Outline each Plasmodium falciparum-infected red blood cell.
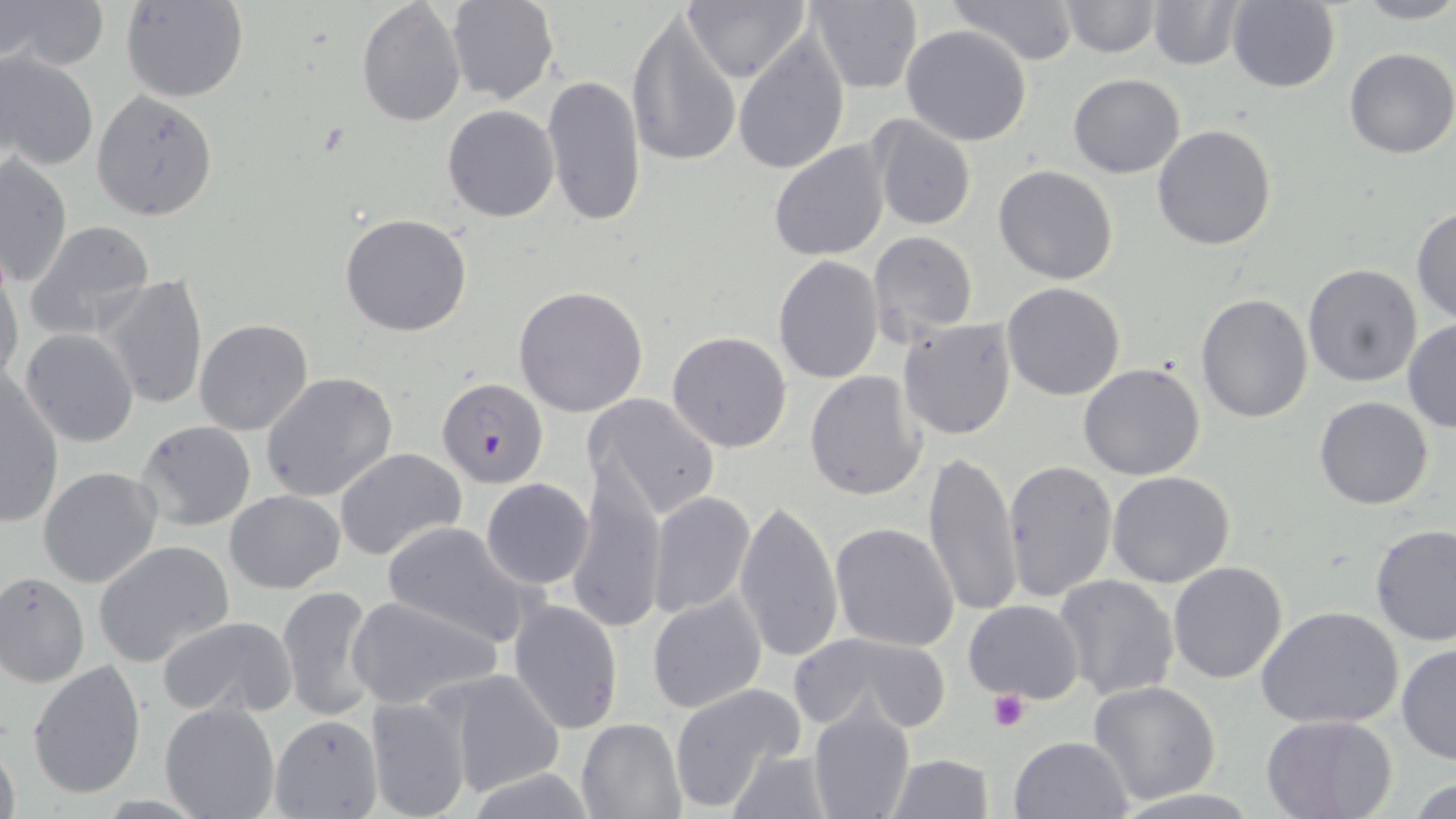
Approximate bounding boxes as named x1/y1/x2/y2 corners in pixels.
Plasmodium falciparum-infected red blood cells (subset): (x1=437, y1=378, x2=549, y2=487).

Uninfected red blood cell locations (subset): (x1=1, y1=0, x2=107, y2=71), (x1=122, y1=0, x2=249, y2=102), (x1=356, y1=0, x2=465, y2=125), (x1=684, y1=0, x2=810, y2=83), (x1=805, y1=0, x2=923, y2=93), (x1=943, y1=0, x2=1080, y2=68), (x1=1058, y1=0, x2=1160, y2=58), (x1=1349, y1=0, x2=1456, y2=25), (x1=447, y1=1, x2=559, y2=104), (x1=1227, y1=1, x2=1342, y2=93), (x1=1149, y1=2, x2=1243, y2=70), (x1=626, y1=10, x2=742, y2=169), (x1=901, y1=23, x2=1032, y2=147), (x1=732, y1=33, x2=850, y2=172), (x1=1344, y1=47, x2=1456, y2=159), (x1=1, y1=50, x2=98, y2=173), (x1=542, y1=72, x2=645, y2=228), (x1=1067, y1=73, x2=1185, y2=178), (x1=90, y1=90, x2=219, y2=221), (x1=442, y1=104, x2=559, y2=222), (x1=867, y1=114, x2=976, y2=230), (x1=1152, y1=124, x2=1277, y2=250), (x1=769, y1=139, x2=891, y2=262), (x1=1, y1=155, x2=72, y2=287), (x1=993, y1=164, x2=1120, y2=285), (x1=1411, y1=207, x2=1456, y2=326), (x1=340, y1=212, x2=473, y2=338), (x1=27, y1=220, x2=155, y2=337), (x1=868, y1=229, x2=978, y2=347), (x1=773, y1=256, x2=884, y2=385), (x1=1302, y1=265, x2=1422, y2=387), (x1=0, y1=268, x2=24, y2=389), (x1=100, y1=275, x2=207, y2=412), (x1=1003, y1=283, x2=1126, y2=401), (x1=513, y1=284, x2=648, y2=417), (x1=1195, y1=293, x2=1314, y2=424), (x1=194, y1=318, x2=314, y2=436), (x1=898, y1=319, x2=1018, y2=440), (x1=1402, y1=319, x2=1456, y2=433), (x1=21, y1=329, x2=138, y2=446), (x1=666, y1=331, x2=793, y2=453), (x1=1079, y1=361, x2=1205, y2=480), (x1=805, y1=371, x2=929, y2=501), (x1=1, y1=373, x2=64, y2=529), (x1=260, y1=373, x2=400, y2=504), (x1=585, y1=392, x2=721, y2=521), (x1=1313, y1=394, x2=1435, y2=510), (x1=134, y1=419, x2=257, y2=531), (x1=334, y1=447, x2=468, y2=562), (x1=922, y1=449, x2=1023, y2=620), (x1=1003, y1=458, x2=1118, y2=603), (x1=565, y1=459, x2=665, y2=631), (x1=38, y1=465, x2=162, y2=588), (x1=1107, y1=471, x2=1236, y2=588), (x1=480, y1=478, x2=595, y2=589), (x1=225, y1=491, x2=345, y2=593), (x1=647, y1=491, x2=756, y2=618), (x1=735, y1=499, x2=844, y2=667), (x1=380, y1=521, x2=538, y2=648), (x1=831, y1=522, x2=960, y2=652), (x1=1369, y1=523, x2=1456, y2=645), (x1=94, y1=541, x2=233, y2=667), (x1=1169, y1=561, x2=1287, y2=684), (x1=0, y1=571, x2=91, y2=685), (x1=1054, y1=575, x2=1179, y2=701), (x1=277, y1=583, x2=383, y2=724), (x1=646, y1=592, x2=767, y2=714), (x1=347, y1=594, x2=501, y2=710), (x1=508, y1=598, x2=624, y2=733), (x1=962, y1=599, x2=1085, y2=704), (x1=1256, y1=605, x2=1404, y2=730), (x1=156, y1=615, x2=299, y2=719), (x1=789, y1=631, x2=951, y2=736), (x1=1396, y1=642, x2=1456, y2=765), (x1=28, y1=659, x2=146, y2=800), (x1=434, y1=669, x2=566, y2=798), (x1=1087, y1=681, x2=1221, y2=805), (x1=666, y1=682, x2=807, y2=812), (x1=365, y1=694, x2=473, y2=819), (x1=159, y1=699, x2=280, y2=819), (x1=808, y1=703, x2=915, y2=819), (x1=1262, y1=714, x2=1396, y2=819), (x1=576, y1=717, x2=686, y2=818), (x1=0, y1=730, x2=20, y2=819), (x1=1009, y1=736, x2=1134, y2=819), (x1=724, y1=748, x2=834, y2=817), (x1=887, y1=752, x2=994, y2=818). Platelet locations: (x1=987, y1=690, x2=1029, y2=733). Slide-level diagnosis: Plasmodium falciparum. Image is 1456×819 pixels. 1000x magnification. Optical microscopy. One field of a larger specimen. May-Grünwald-Giemsa-stained preparation. Thin blood smear.